Assess the morphology of the red blood cells.
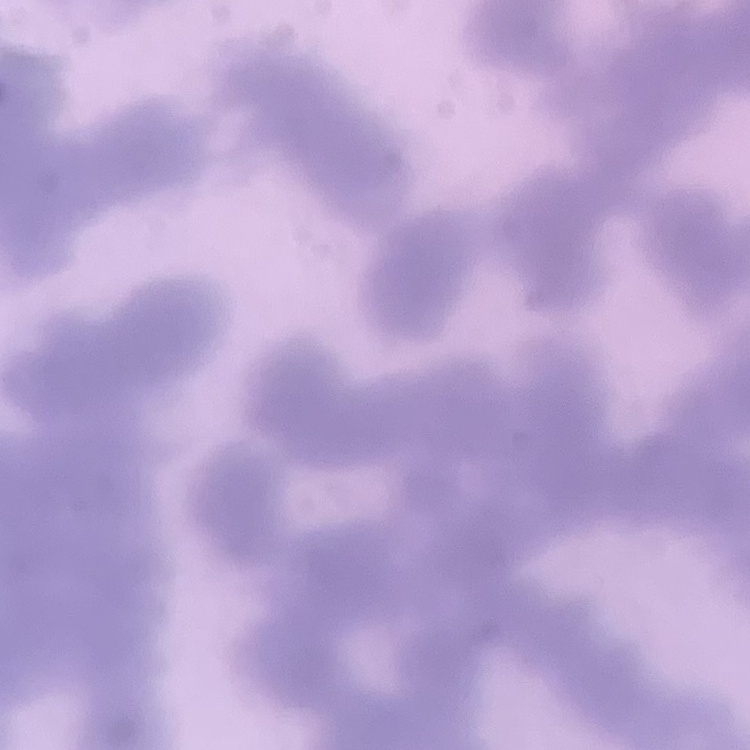

Rouleaux formation.

preparation = thin blood film
stain = Field's or Giemsa
image type = one tile cut from a larger photomicrograph